Give the extent of all uninfected red blood cells.
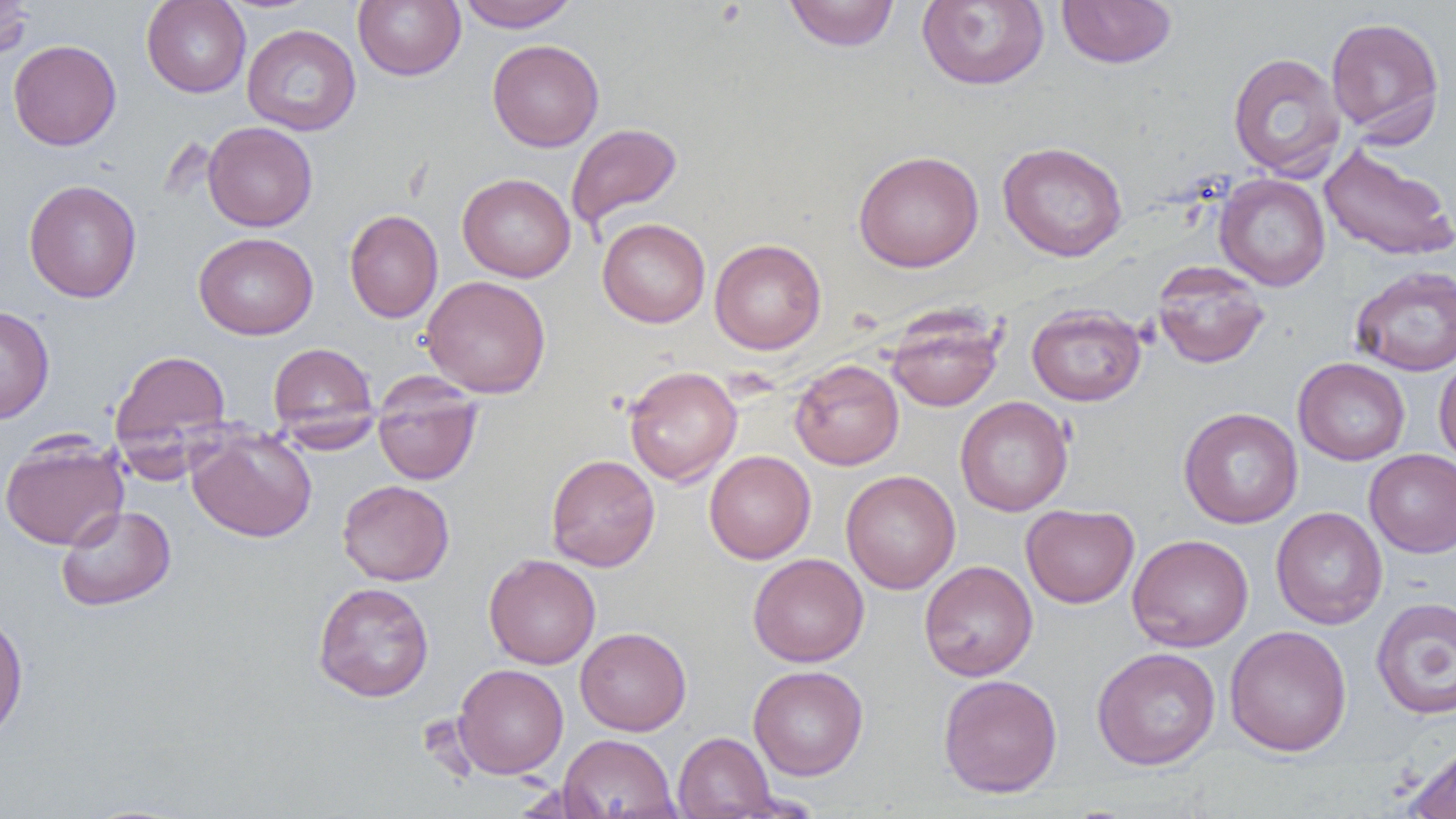

Approximate bounding boxes as [x1, y1, x2, y2] in pixels.
Uninfected red blood cells: [0, 0, 34, 60], [141, 0, 251, 98], [353, 0, 466, 81], [457, 0, 577, 31], [783, 0, 900, 52], [1056, 0, 1177, 68], [917, 1, 1048, 89], [1325, 16, 1445, 143], [242, 24, 361, 136], [487, 38, 604, 152], [8, 39, 121, 151], [1227, 52, 1346, 179], [202, 121, 317, 232], [565, 122, 683, 233], [997, 141, 1128, 262], [1319, 144, 1456, 262], [853, 150, 984, 272], [458, 173, 575, 282], [1214, 173, 1331, 291], [23, 179, 142, 303], [344, 209, 443, 323], [597, 218, 711, 328], [193, 232, 318, 340], [709, 238, 826, 355], [1152, 261, 1270, 369], [1351, 265, 1456, 375], [421, 275, 551, 398], [1026, 304, 1147, 406], [0, 305, 55, 424], [886, 307, 1004, 412], [268, 342, 379, 444], [110, 348, 232, 461], [1434, 356, 1456, 467], [1293, 357, 1410, 465], [789, 359, 904, 470], [623, 365, 742, 486], [372, 377, 483, 485], [955, 396, 1073, 516], [1178, 407, 1303, 528], [186, 426, 317, 543], [1, 432, 129, 549], [1364, 449, 1456, 557], [704, 450, 815, 564], [546, 454, 660, 571], [841, 470, 960, 594], [337, 479, 455, 586], [1021, 503, 1139, 608], [56, 505, 176, 611], [1271, 506, 1387, 629], [1127, 534, 1253, 652], [484, 553, 601, 670], [747, 553, 869, 667], [919, 560, 1038, 681], [312, 582, 434, 702], [1370, 597, 1456, 719], [0, 612, 29, 742], [1224, 625, 1352, 756], [575, 626, 691, 735], [1091, 647, 1221, 770], [453, 663, 569, 779], [748, 665, 868, 780], [938, 674, 1063, 798], [673, 732, 776, 819], [558, 733, 679, 818], [1404, 743, 1456, 819].

slide-level diagnosis = no evidence of blood parasites
field of view = single
preparation = thin blood smear
modality = light microscopy
image size = 1456×819 pixels
magnification = 1000x